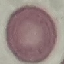
Summary:
  - Malaria status: uninfected
  - Preparation: thin blood film
  - Image type: automatically extracted cell patch, resized to 64 × 64 pixels
  - Capture: smartphone through the microscope eyepiece
  - Stain: Giemsa